State which parasite is depicted.
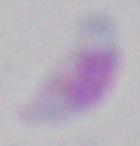
This is Toxoplasma gondii.

modality = micrograph
magnification = 1000x